Report the malaria status of this cell.
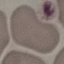
It is uninfected.

Photographed with a smartphone camera at the microscope eyepiece. Cell patch, automatically extracted from a larger field of view and resized to 64 × 64 pixels. Giemsa-stained preparation. Thin blood smear.